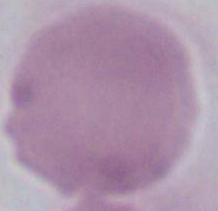
An erythrocyte is seen. 1000x magnification. Micrograph.